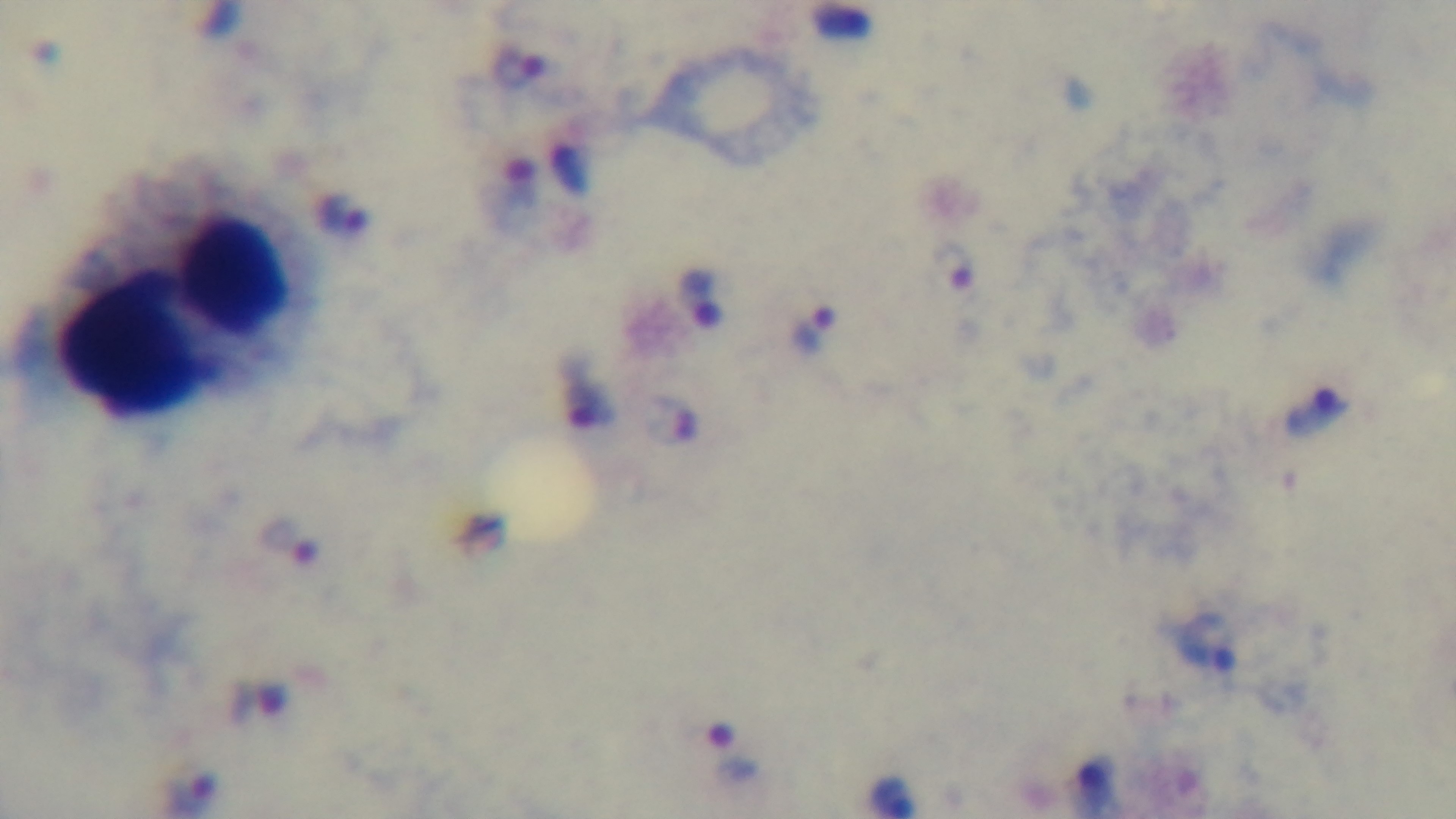
modality = light microscopy
objective = 100x oil immersion
stain = Giemsa
malaria status = infected
capture = mounted 4K digital camera
preparation = thick blood film
field of view = one from the slide